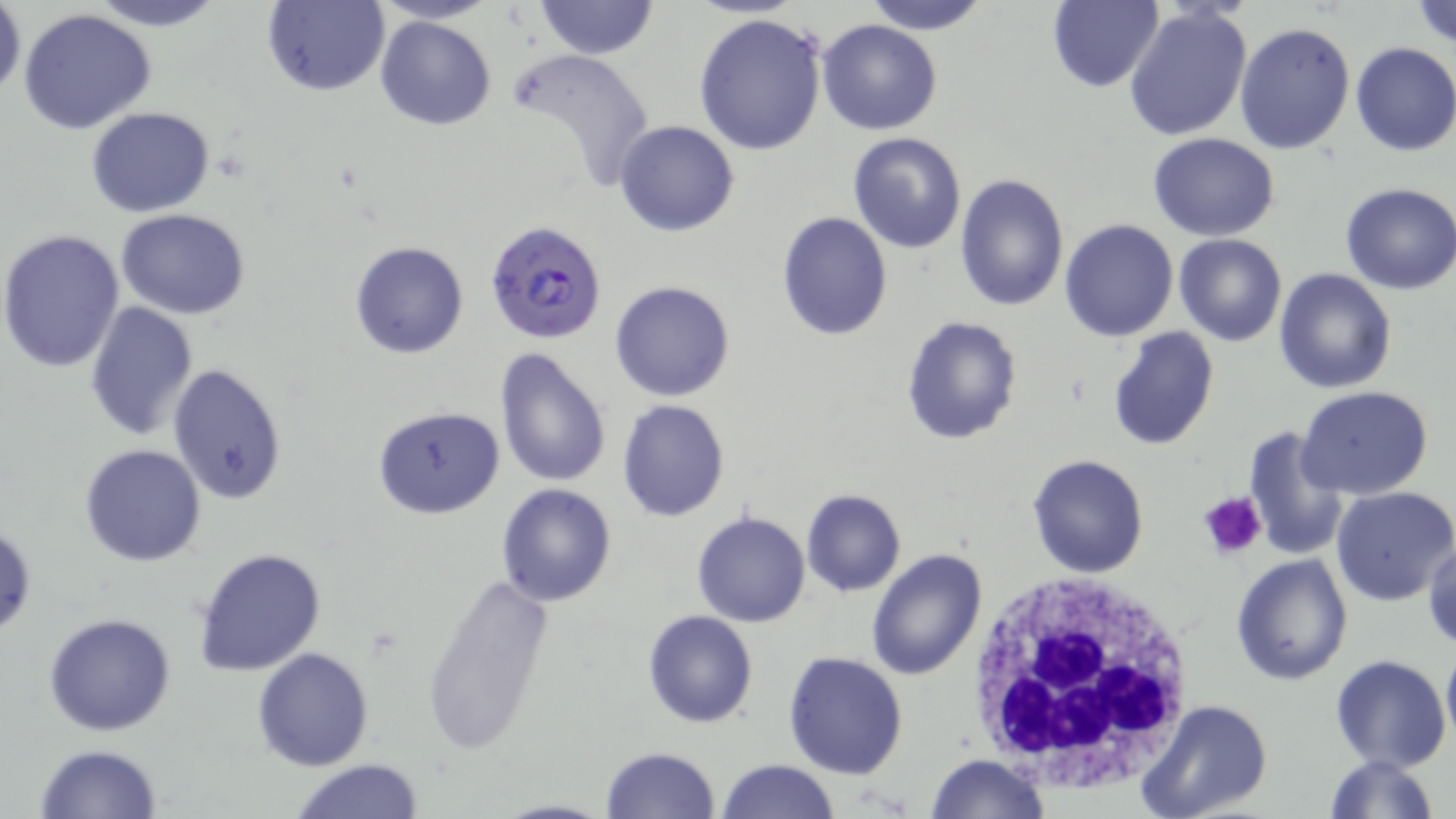 Approximate bounding boxes as (x1,y1)-(x2,y2) corner pairs in pixels. Platelet locations: (1198,491)-(1267,562). White blood cell locations: (962,571)-(1200,793). Plasmodium falciparum-infected red blood cell locations: (485,220)-(608,344). Uninfected red blood cell locations: (87,0)-(227,31), (366,0)-(501,26), (533,0)-(657,59), (862,0)-(992,34), (1412,0)-(1456,49), (262,1)-(387,96), (1047,1)-(1164,92), (0,2)-(25,100), (1124,4)-(1254,143), (19,9)-(156,136), (693,12)-(828,157), (375,16)-(495,131), (817,18)-(942,134), (1234,21)-(1358,156), (1350,41)-(1456,157), (509,47)-(655,196), (86,106)-(216,217), (614,119)-(740,237), (848,132)-(966,254), (1148,132)-(1279,240), (954,173)-(1069,310), (1340,182)-(1456,296), (115,207)-(250,319), (776,211)-(892,340), (1060,218)-(1179,340), (0,230)-(126,374), (1174,234)-(1286,346), (349,241)-(469,360), (1274,268)-(1397,394), (610,279)-(737,401), (83,300)-(199,440), (901,315)-(1023,445), (1106,326)-(1220,451), (495,349)-(611,488), (167,366)-(288,506), (1296,386)-(1434,500), (616,398)-(731,523), (372,405)-(505,519), (1242,425)-(1348,561), (79,444)-(207,567), (1026,453)-(1149,578), (495,484)-(617,606), (1329,485)-(1456,607), (800,489)-(906,596), (691,510)-(811,628), (0,523)-(37,642), (1424,537)-(1456,653), (193,547)-(326,677), (865,548)-(988,683), (1231,553)-(1354,687), (421,571)-(553,756), (643,611)-(758,729), (43,612)-(176,737), (1441,637)-(1456,753), (252,646)-(375,770), (783,651)-(908,777), (1330,653)-(1453,773), (1136,698)-(1274,819), (33,742)-(164,818), (599,745)-(722,818), (1323,753)-(1441,819), (926,754)-(1050,818), (289,758)-(428,818), (716,759)-(838,818), (492,799)-(617,819). Slide-level diagnosis: Plasmodium falciparum. Image is 1456×819 pixels. Thin blood film. Light microscopy. One field of a larger specimen. May-Grünwald-Giemsa-stained preparation. 1000x magnification.